Locate and identify every blood parasite.
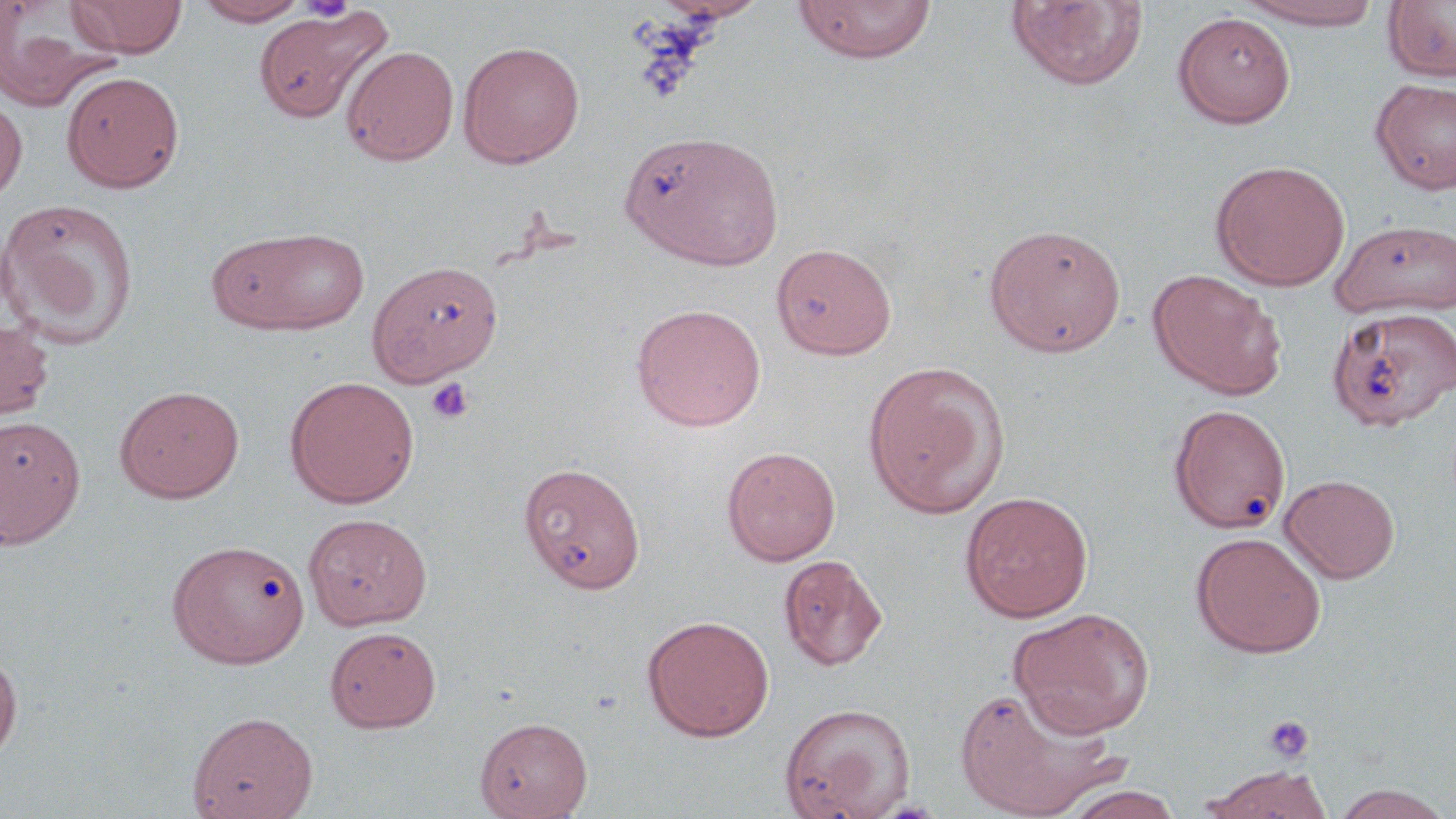

No blood parasites observed.

Approximate bounding boxes as (x1,y1)-(x2,y2) corner pairs in pixels. Uninfected red blood cell locations: (66,0)-(188,58), (194,0)-(311,26), (653,0)-(768,24), (790,0)-(937,63), (1005,0)-(1150,92), (1235,0)-(1388,30), (1383,1)-(1456,82), (0,4)-(116,111), (253,5)-(394,124), (1172,11)-(1296,128), (458,40)-(585,168), (341,45)-(460,166), (61,70)-(184,192), (1371,77)-(1456,195), (0,94)-(27,207), (619,130)-(781,269), (1210,159)-(1350,291), (0,197)-(140,346), (1331,219)-(1456,319), (983,223)-(1127,357), (210,226)-(371,335), (771,242)-(897,360), (371,261)-(508,387), (1147,268)-(1287,399), (631,303)-(767,432), (1327,306)-(1456,432), (0,317)-(55,420), (862,360)-(1011,519), (284,375)-(420,509), (115,385)-(244,502), (1169,403)-(1291,533), (0,415)-(86,548), (721,446)-(841,566), (518,461)-(646,594), (1280,474)-(1401,583), (959,491)-(1094,622), (303,513)-(432,630), (1190,531)-(1327,658), (167,539)-(310,668), (778,553)-(888,671), (1009,607)-(1155,738), (642,614)-(775,742), (325,626)-(441,732), (0,647)-(22,763), (954,683)-(1123,818), (778,701)-(917,819), (187,710)-(318,819), (474,716)-(592,818), (1198,765)-(1333,819), (1327,783)-(1456,818), (1062,786)-(1183,819). Platelet locations: (298,0)-(357,22), (425,377)-(475,424), (1262,714)-(1314,764). Slide-level diagnosis: no evidence of blood parasites. Thin blood smear. May-Grünwald-Giemsa stain. Image is 1456×819 pixels. One field of a larger specimen. Optical microscopy. Captured at 1000x magnification.